Classify this cell by malaria status.
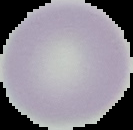

Uninfected.

preparation = thin blood smear
image size = 133×130 pixels
image type = segmented cell region with the area outside set to black